Identify the blood parasite species.
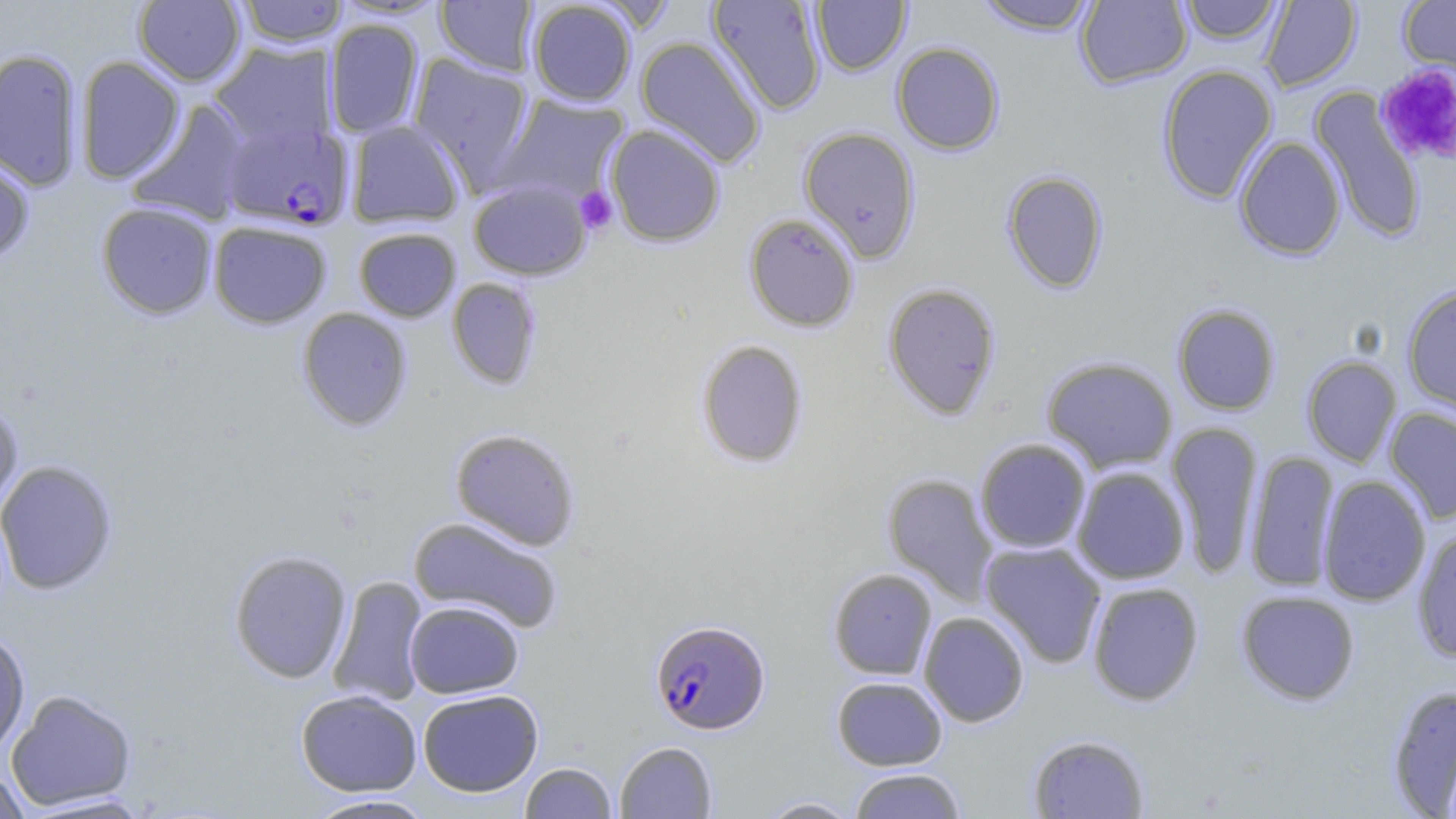
Plasmodium falciparum.

Summary:
  - Coordinate format: approximate bounding boxes as named x1/y1/x2/y2 corners in pixels
  - Plasmodium falciparum-infected red blood cell locations: (x1=220, y1=121, x2=354, y2=231), (x1=650, y1=619, x2=770, y2=734)
  - Platelet locations: (x1=1375, y1=63, x2=1456, y2=166), (x1=575, y1=185, x2=618, y2=235)
  - Uninfected red blood cell locations: (x1=236, y1=0, x2=347, y2=47), (x1=436, y1=0, x2=539, y2=76), (x1=707, y1=0, x2=827, y2=115), (x1=975, y1=0, x2=1098, y2=35), (x1=1075, y1=0, x2=1193, y2=88), (x1=1178, y1=0, x2=1284, y2=44), (x1=1259, y1=0, x2=1361, y2=92), (x1=1399, y1=0, x2=1456, y2=81), (x1=133, y1=1, x2=246, y2=86), (x1=527, y1=1, x2=637, y2=106), (x1=811, y1=1, x2=911, y2=76), (x1=324, y1=18, x2=424, y2=138), (x1=635, y1=36, x2=766, y2=168), (x1=211, y1=41, x2=336, y2=148), (x1=891, y1=41, x2=1004, y2=155), (x1=0, y1=48, x2=84, y2=192), (x1=408, y1=53, x2=535, y2=191), (x1=74, y1=56, x2=185, y2=184), (x1=1157, y1=64, x2=1277, y2=204), (x1=1310, y1=88, x2=1427, y2=244), (x1=493, y1=93, x2=630, y2=207), (x1=125, y1=99, x2=252, y2=226), (x1=346, y1=120, x2=466, y2=228), (x1=605, y1=124, x2=725, y2=247), (x1=798, y1=126, x2=921, y2=262), (x1=1234, y1=135, x2=1346, y2=260), (x1=0, y1=152, x2=36, y2=265), (x1=1001, y1=170, x2=1108, y2=294), (x1=468, y1=179, x2=592, y2=280), (x1=96, y1=202, x2=218, y2=320), (x1=743, y1=212, x2=860, y2=332), (x1=208, y1=220, x2=332, y2=328), (x1=353, y1=226, x2=461, y2=322), (x1=446, y1=277, x2=542, y2=389), (x1=882, y1=282, x2=1001, y2=420), (x1=1401, y1=283, x2=1456, y2=416), (x1=1173, y1=304, x2=1280, y2=415), (x1=297, y1=307, x2=412, y2=431), (x1=696, y1=340, x2=808, y2=468), (x1=1041, y1=356, x2=1178, y2=473), (x1=1301, y1=356, x2=1402, y2=467), (x1=0, y1=399, x2=24, y2=514), (x1=1384, y1=406, x2=1456, y2=524), (x1=1166, y1=420, x2=1263, y2=579), (x1=450, y1=428, x2=580, y2=550), (x1=975, y1=438, x2=1091, y2=554), (x1=1245, y1=449, x2=1340, y2=593), (x1=0, y1=459, x2=119, y2=596), (x1=1071, y1=466, x2=1190, y2=584), (x1=882, y1=473, x2=998, y2=605), (x1=1317, y1=475, x2=1431, y2=607), (x1=408, y1=515, x2=563, y2=633), (x1=1412, y1=527, x2=1456, y2=663), (x1=980, y1=541, x2=1107, y2=668), (x1=229, y1=550, x2=352, y2=683), (x1=828, y1=568, x2=937, y2=679), (x1=327, y1=575, x2=428, y2=707), (x1=1087, y1=581, x2=1204, y2=706), (x1=1236, y1=590, x2=1361, y2=705), (x1=405, y1=600, x2=524, y2=698), (x1=919, y1=611, x2=1030, y2=727), (x1=0, y1=629, x2=30, y2=758), (x1=832, y1=676, x2=947, y2=770), (x1=1386, y1=684, x2=1456, y2=817), (x1=6, y1=689, x2=137, y2=811), (x1=418, y1=689, x2=543, y2=796), (x1=296, y1=690, x2=422, y2=795), (x1=1028, y1=734, x2=1150, y2=818), (x1=615, y1=741, x2=717, y2=818), (x1=520, y1=762, x2=617, y2=819), (x1=1, y1=766, x2=30, y2=819), (x1=847, y1=768, x2=966, y2=818), (x1=17, y1=791, x2=157, y2=817), (x1=303, y1=794, x2=439, y2=818), (x1=755, y1=796, x2=863, y2=818)
  - Stain: May-Grünwald-Giemsa
  - Magnification: 1000x
  - Preparation: thin blood film
  - Modality: optical microscopy
  - Image size: 1456×819 pixels
  - Field of view: single